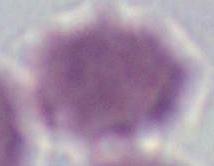
Summary:
  - Modality: photomicrograph
  - Magnification: 1000x
  - Identification: red blood cell